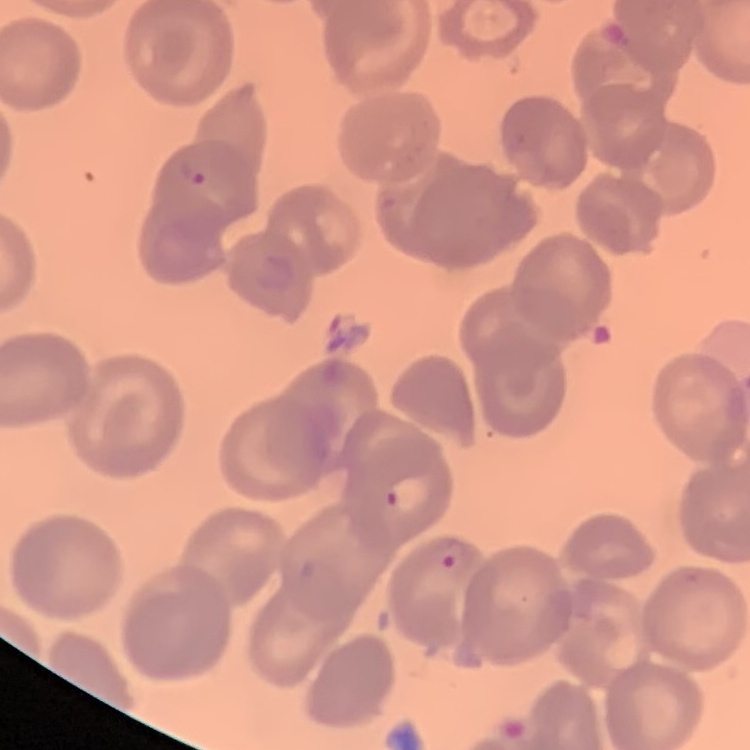
Summary:
  - Erythrocyte morphology: no rouleaux formation
  - Stain: Field's or Giemsa
  - Preparation: thin blood film
  - Image type: square crop of a larger photomicrograph